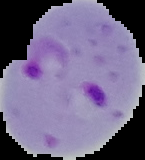

Summary:
  - Image size: 145×160 pixels
  - Preparation: thin blood smear
  - Image type: segmented cell region on a black background
  - Malaria status: parasitized